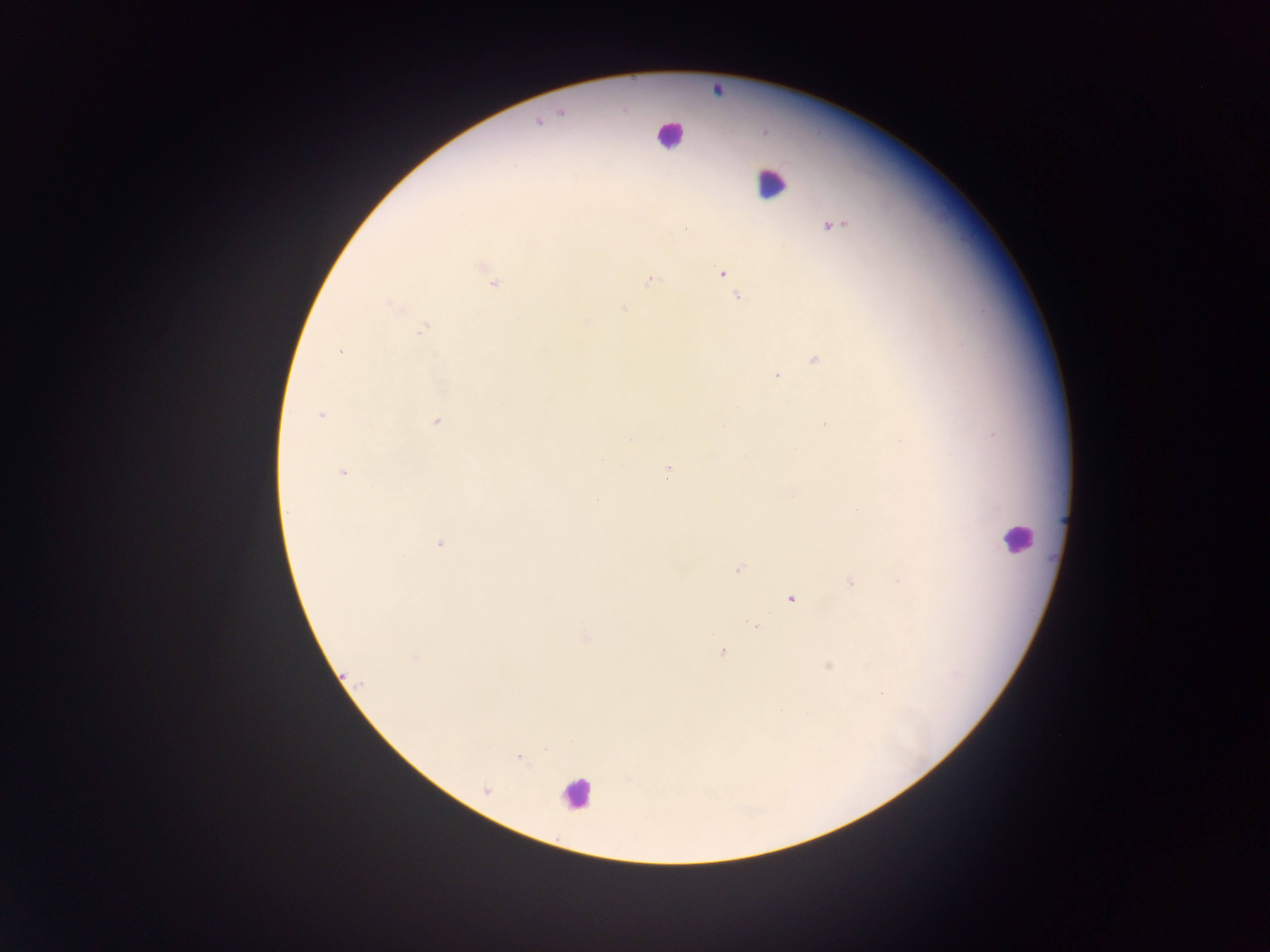

Approximate centers as {x, y} in pixels.
Summary:
  - Plasmodium parasite locations: {561, 111}, {537, 122}, {833, 225}, {723, 274}, {649, 280}, {493, 282}, {737, 296}, {624, 308}, {585, 321}, {421, 329}, {339, 352}, {775, 375}, {737, 407}, {320, 415}, {436, 421}, {823, 423}, {343, 472}, {665, 472}, {790, 495}, {440, 544}, {738, 569}, {900, 579}, {849, 580}, {790, 598}, {756, 625}, {585, 637}, {722, 650}, {415, 659}, {519, 757}
  - Leukocyte locations: {667, 137}, {772, 182}, {1014, 537}, {578, 795}
  - Image size: 1270×952 pixels
  - Country: Ghana
  - Preparation: thick blood film
  - Field of view: single
  - Capture: mobile-phone photograph through a microscope